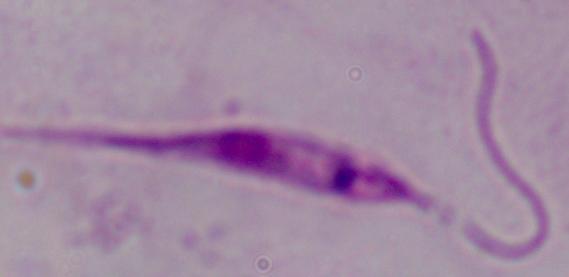
Summary:
  - Modality: photomicrograph
  - Magnification: 1000x
  - Identification: Leishmania